Mark where platelets are.
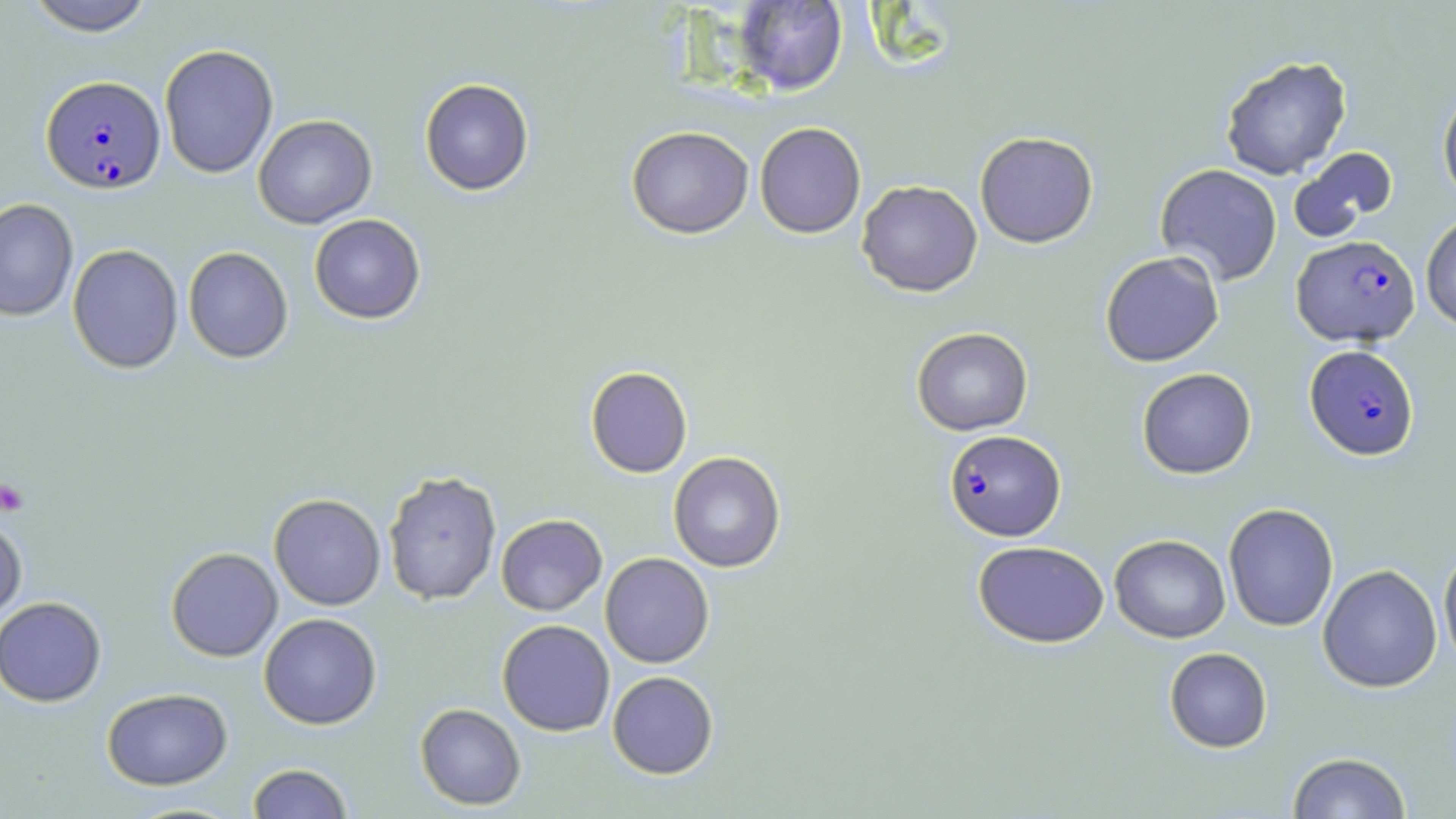
Approximate bounding boxes as [x1, y1, x2, y2] in pixels.
Platelets: [0, 477, 30, 517].

slide-level diagnosis = Plasmodium falciparum
field of view = one of a larger specimen
uninfected red blood cell locations = approximate bounding boxes as [x1, y1, x2, y2] in pixels: [24, 0, 156, 36], [731, 1, 848, 95], [159, 44, 279, 178], [1220, 55, 1352, 180], [419, 78, 534, 196], [1438, 87, 1456, 206], [253, 114, 377, 229], [754, 122, 867, 239], [626, 125, 754, 239], [974, 131, 1098, 248], [1289, 146, 1398, 243], [1155, 164, 1283, 285], [856, 180, 983, 297], [0, 198, 78, 321], [1421, 212, 1456, 330], [309, 213, 426, 324], [67, 244, 184, 374], [183, 246, 293, 363], [1100, 251, 1224, 367], [911, 326, 1033, 436], [585, 366, 693, 478], [1137, 367, 1257, 479], [668, 451, 786, 573], [382, 470, 502, 606], [269, 493, 386, 610], [1223, 503, 1339, 632], [0, 514, 28, 627], [495, 514, 608, 616], [1109, 534, 1231, 643], [973, 540, 1110, 648], [1438, 546, 1456, 671], [165, 547, 283, 662], [600, 552, 715, 668], [1318, 564, 1442, 693], [0, 596, 107, 707], [259, 613, 382, 729], [497, 619, 615, 736], [1164, 647, 1272, 753], [607, 670, 718, 779], [101, 687, 232, 790], [415, 703, 526, 810], [1287, 752, 1412, 818], [247, 763, 354, 819]
image size = 1456×819 pixels
stain = May-Grünwald-Giemsa
magnification = 1000x
Plasmodium falciparum-infected red blood cell locations = approximate bounding boxes as [x1, y1, x2, y2] in pixels: [41, 76, 165, 193], [1292, 235, 1420, 346], [1305, 344, 1419, 460], [943, 429, 1066, 541]
modality = optical microscopy
preparation = thin blood film